Assess this cell for malaria.
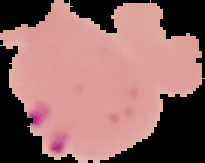
It is parasitized.

Image is 205×163 pixels. The area outside the segmented cell region is set to black. From a thin blood smear.